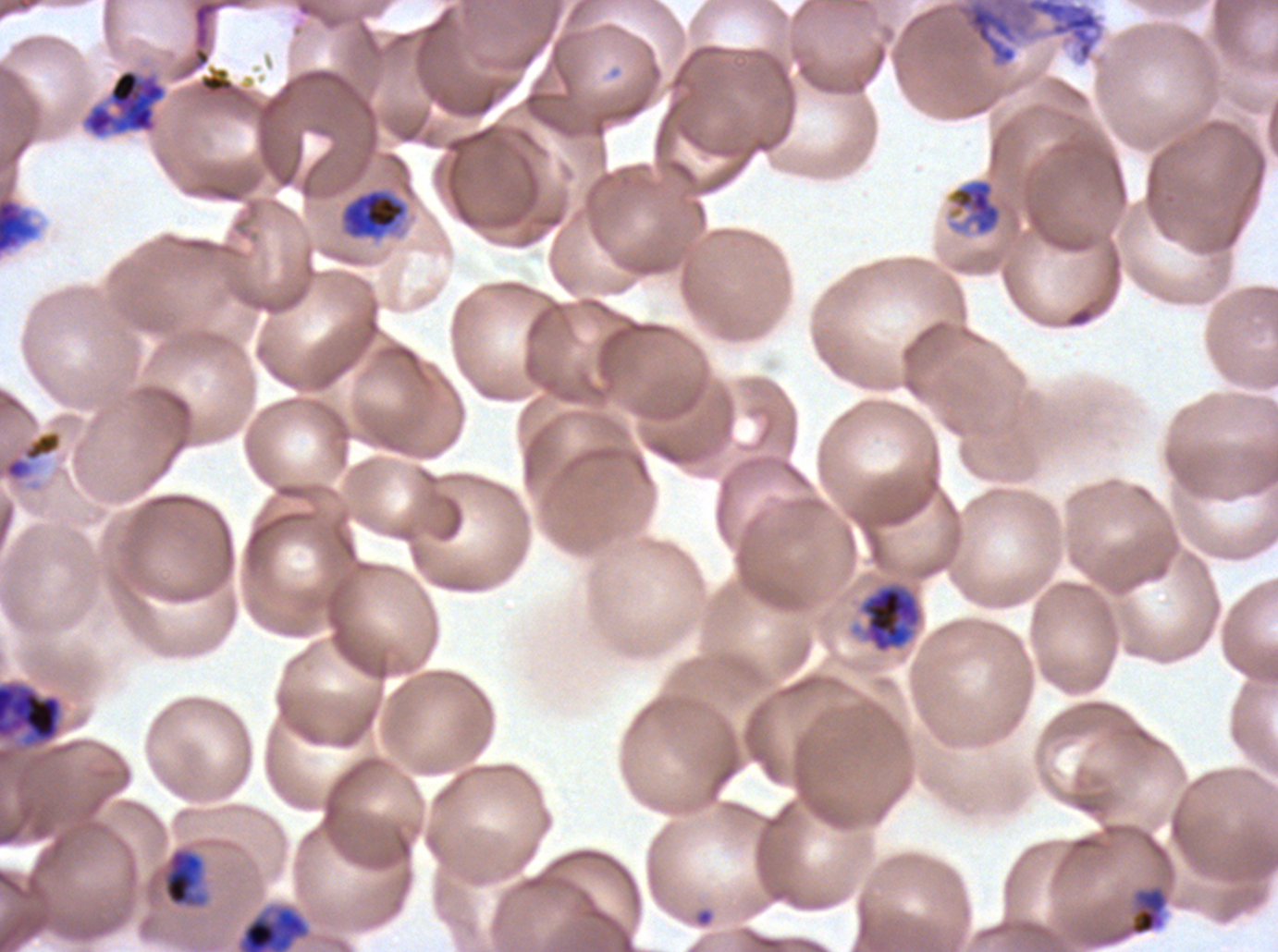

notation = approximate bounding boxes as {x1, y1, x2, y2} in pixels
debris locations = {172, 0, 250, 82}, {953, 0, 1104, 67}
mid trophozoite locations = {947, 177, 1003, 237}, {161, 846, 209, 909}, {236, 904, 311, 951}
late-ring/early-trophozoite locations = {1092, 882, 1171, 948}
ring locations = {692, 906, 716, 929}
early schizont locations = {82, 68, 166, 139}, {0, 196, 37, 255}, {859, 582, 923, 653}
late schizont locations = {0, 679, 64, 750}
late trophozoite locations = {338, 187, 410, 243}, {0, 429, 63, 483}
specimen = ex-vivo Plasmodium falciparum culture from a patient in The Gambia, grown for 24 to 48 hours
preparation = thin blood smear
life-cycle stages observed = ring, late-ring/early-trophozoite, mid trophozoite, late trophozoite, early schizont, late schizont
stain = Giemsa
field of view = one sub-image of a larger composite
image size = 1278×952 pixels